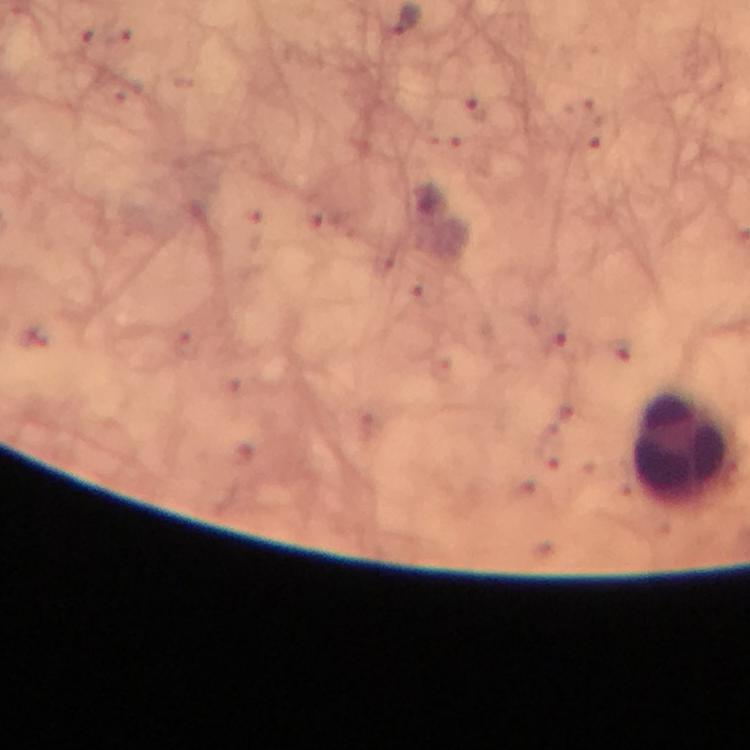 Approximate centers as (x, y) in pixels. Malaria parasite locations: (477, 110). Leukocyte locations: (688, 448). Thick blood film. From a diagnostic examination for malaria. Immersion oil applied. Image is 750×750 pixels. 100x magnification. Giemsa stain. Photographed with a smartphone mounted on the microscope. A crop from one field of view.